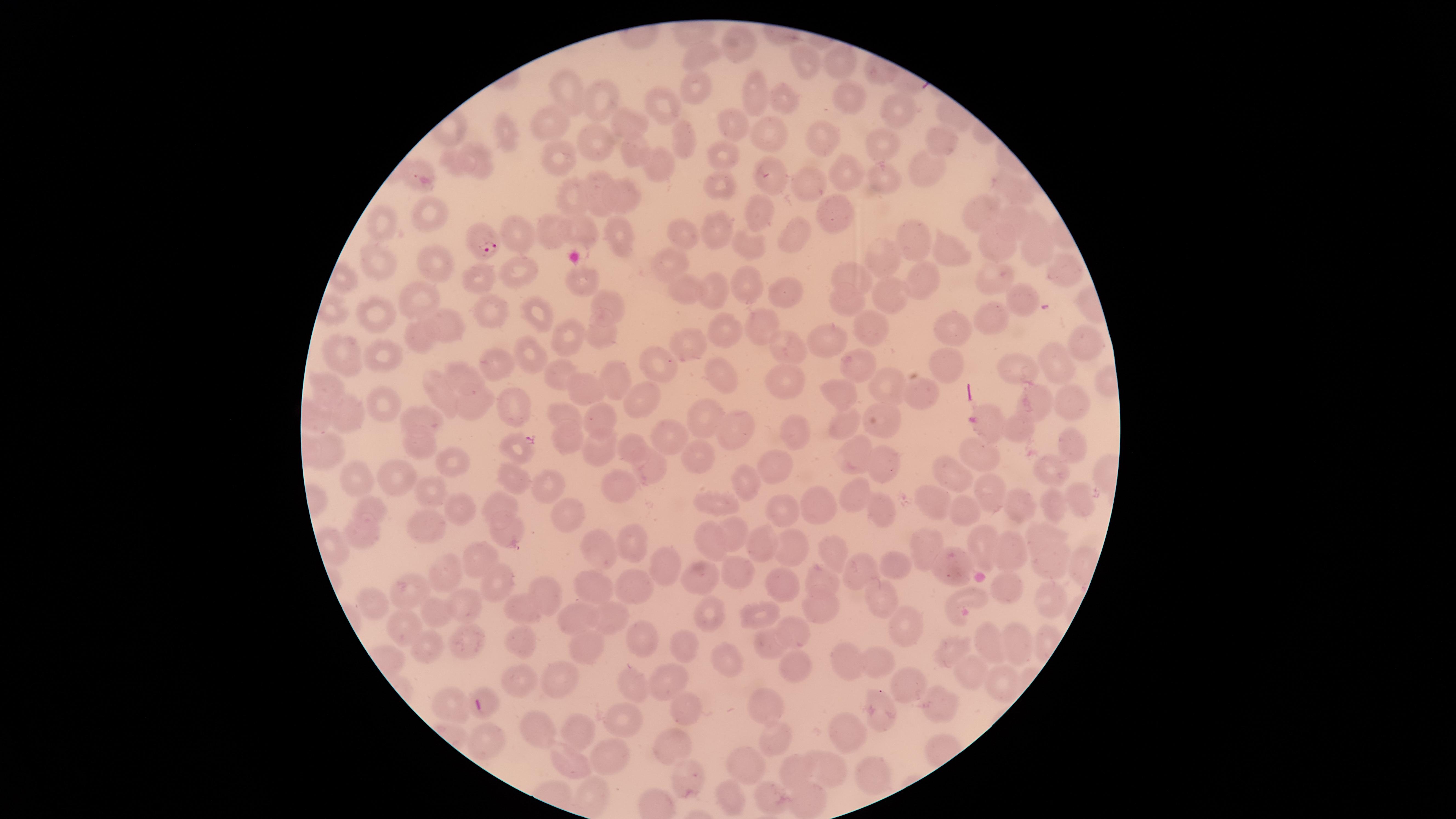
capture = smartphone photograph through the microscope eyepiece
field of view = single
presence = malaria parasites detected
preparation = thin smear of blood
image size = 1456×819 pixels
stain = Giemsa
visible region = circular
species = Plasmodium falciparum
parasitized red blood cells = approximate marker points as (x, y) in pixels: (484, 242)
uninfected red blood cells = approximate marker points as (x, y) in pixels: (733, 44), (699, 53), (806, 63), (839, 67), (695, 88), (754, 89), (569, 90), (844, 96), (780, 97), (599, 99), (665, 102), (893, 105), (729, 121), (550, 122), (632, 123), (769, 134), (504, 136), (817, 138), (941, 138), (593, 139), (682, 139), (884, 146), (631, 149), (722, 156), (556, 157), (481, 159), (659, 163), (924, 167), (411, 172), (846, 174), (879, 174), (766, 176), (715, 185), (804, 186), (1009, 187), (598, 193), (625, 195), (574, 199), (835, 207), (979, 210), (434, 213), (754, 215), (1015, 216), (384, 221), (715, 226), (1039, 226), (580, 229), (552, 230), (794, 233), (913, 233), (520, 234), (617, 235), (678, 236), (992, 240), (748, 247), (1039, 248), (953, 250), (880, 258), (431, 262), (384, 263), (667, 263), (1066, 267), (524, 268), (845, 276), (483, 277), (996, 277), (923, 280), (579, 283), (749, 285), (679, 286), (714, 292), (780, 292), (1021, 295), (886, 296), (418, 297), (606, 304), (843, 304), (491, 312), (535, 315), (378, 316), (995, 319), (762, 321), (444, 325), (725, 325), (869, 327), (602, 328), (959, 330), (571, 332), (421, 333), (1087, 341), (827, 344), (688, 345), (786, 349), (383, 353), (530, 353), (344, 354), (858, 361), (1059, 361), (659, 363), (498, 364), (946, 366), (1019, 368), (611, 372), (717, 377), (559, 378), (786, 380), (464, 381), (883, 385), (581, 386), (444, 390), (327, 391), (842, 392), (915, 394), (1040, 398), (1070, 398), (512, 401), (648, 402), (471, 405), (387, 407), (346, 413), (881, 415), (561, 416), (602, 419), (711, 419), (418, 420), (844, 421), (988, 424), (1015, 427), (738, 428), (792, 429), (569, 434), (666, 436), (514, 443), (1069, 445), (422, 446), (631, 448), (329, 449), (598, 450), (699, 451), (853, 455), (983, 456), (455, 461), (883, 461), (646, 467), (772, 467), (1050, 471), (955, 477), (394, 478), (513, 478), (360, 480), (743, 482), (550, 484), (623, 484), (989, 490), (430, 491), (858, 493), (1077, 497), (931, 499), (816, 501), (714, 502), (1018, 503), (495, 505), (1057, 506), (371, 507), (461, 508), (968, 510), (782, 511), (571, 515), (883, 516), (424, 522), (502, 531), (735, 534), (1038, 535), (365, 538), (765, 542), (714, 543), (634, 545), (920, 545), (986, 546), (793, 548), (832, 550), (598, 551), (1008, 551), (474, 557), (1049, 559), (663, 561), (894, 561), (953, 566), (855, 568), (444, 572), (732, 573), (823, 577), (697, 578), (500, 582), (635, 582), (789, 583), (406, 584), (598, 586), (545, 590), (1007, 591), (883, 593), (1051, 598), (966, 600), (464, 604), (823, 604), (369, 605), (526, 607), (759, 612), (437, 614), (706, 614), (577, 617), (607, 619), (906, 624), (798, 631), (403, 632), (643, 638), (1016, 642), (467, 643), (522, 643), (774, 644), (992, 645), (681, 647), (586, 648), (951, 648), (429, 653), (727, 659), (876, 659), (844, 664), (793, 666), (966, 672), (667, 677), (557, 680), (521, 682), (1000, 683), (635, 685), (912, 685), (450, 701), (939, 702), (770, 705), (682, 706), (485, 708), (877, 712), (623, 718), (537, 730), (844, 731), (581, 732), (486, 738), (772, 741), (669, 748), (614, 759), (743, 762), (569, 765), (825, 771), (793, 774), (682, 775), (872, 779), (588, 794), (724, 797), (769, 799), (803, 800)